Locate every blood parasite and identify its species.
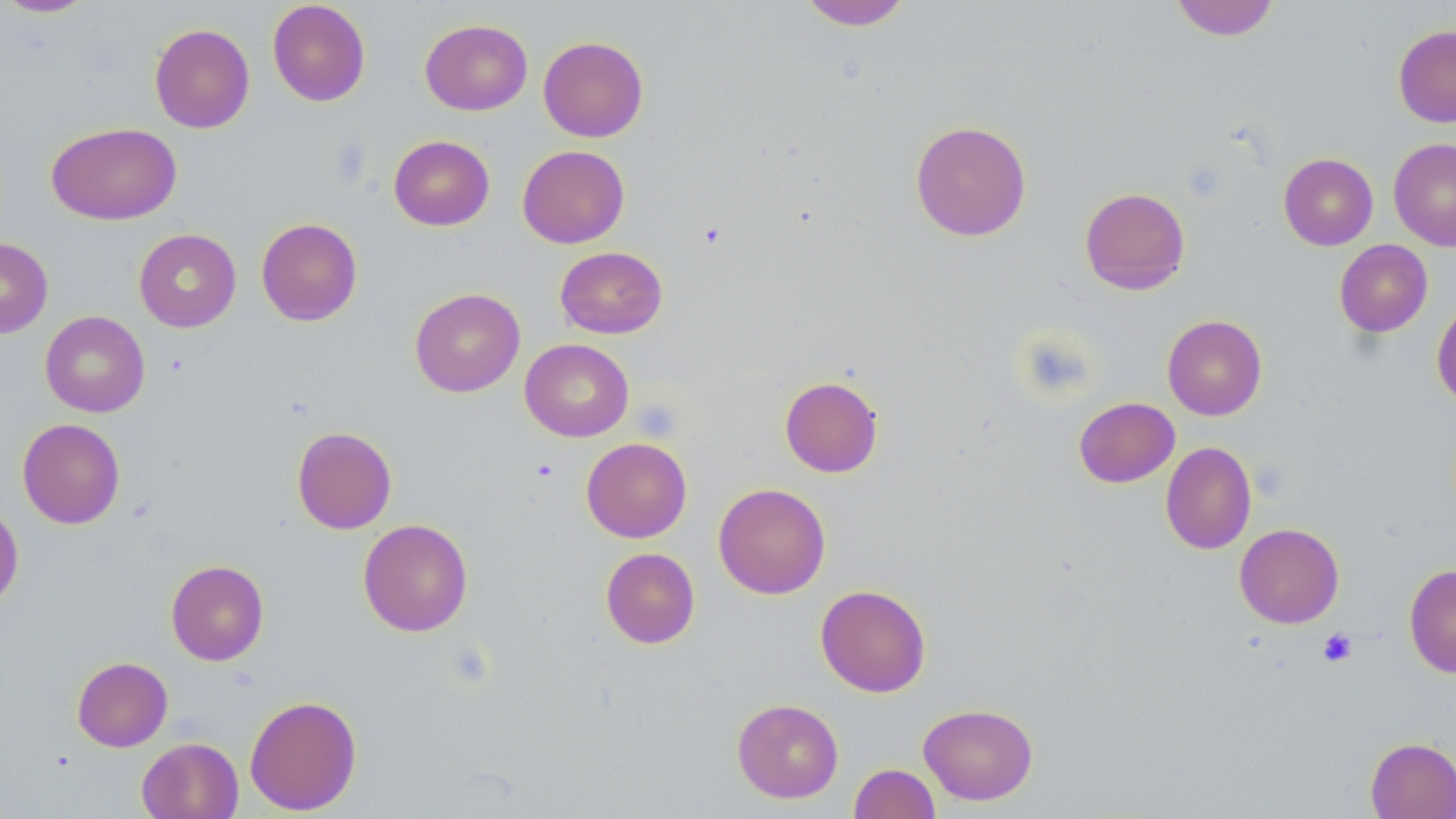
No blood parasites seen.

Summary:
  - Coordinate format: approximate bounding boxes as named x1/y1/x2/y2 corners in pixels
  - Uninfected red blood cell locations: (x1=0, y1=0, x2=97, y2=18), (x1=799, y1=0, x2=912, y2=30), (x1=1170, y1=0, x2=1279, y2=41), (x1=267, y1=1, x2=371, y2=106), (x1=420, y1=19, x2=533, y2=116), (x1=149, y1=23, x2=255, y2=133), (x1=1393, y1=25, x2=1456, y2=127), (x1=538, y1=36, x2=649, y2=142), (x1=909, y1=120, x2=1031, y2=242), (x1=46, y1=122, x2=181, y2=225), (x1=388, y1=135, x2=495, y2=231), (x1=1389, y1=138, x2=1456, y2=250), (x1=517, y1=145, x2=630, y2=248), (x1=1279, y1=153, x2=1378, y2=250), (x1=1080, y1=187, x2=1190, y2=294), (x1=256, y1=218, x2=362, y2=326), (x1=134, y1=226, x2=361, y2=327), (x1=134, y1=228, x2=241, y2=332), (x1=0, y1=237, x2=53, y2=338), (x1=1334, y1=239, x2=1433, y2=337), (x1=555, y1=246, x2=668, y2=339), (x1=410, y1=287, x2=525, y2=397), (x1=1431, y1=299, x2=1456, y2=409), (x1=40, y1=310, x2=150, y2=417), (x1=1162, y1=315, x2=1267, y2=420), (x1=520, y1=339, x2=634, y2=442), (x1=779, y1=375, x2=883, y2=478), (x1=1074, y1=397, x2=1179, y2=487), (x1=17, y1=418, x2=125, y2=529), (x1=292, y1=426, x2=397, y2=533), (x1=581, y1=437, x2=692, y2=543), (x1=1161, y1=442, x2=1256, y2=555), (x1=713, y1=483, x2=831, y2=599), (x1=0, y1=502, x2=23, y2=611), (x1=358, y1=519, x2=473, y2=636), (x1=1234, y1=523, x2=1344, y2=628), (x1=600, y1=547, x2=700, y2=649), (x1=166, y1=560, x2=269, y2=665), (x1=1404, y1=563, x2=1456, y2=678), (x1=815, y1=584, x2=931, y2=697), (x1=72, y1=656, x2=172, y2=752), (x1=244, y1=694, x2=362, y2=815), (x1=732, y1=698, x2=844, y2=803), (x1=918, y1=703, x2=1038, y2=805), (x1=136, y1=737, x2=244, y2=819), (x1=1365, y1=737, x2=1456, y2=818), (x1=849, y1=763, x2=940, y2=819)
  - Platelet locations: (x1=532, y1=458, x2=559, y2=482), (x1=1317, y1=628, x2=1357, y2=667)
  - Slide-level diagnosis: negative for blood parasites
  - Image size: 1456×819 pixels
  - Modality: optical microscopy
  - Preparation: thin blood smear
  - Magnification: 1000x
  - Field of view: single
  - Stain: May-Grünwald-Giemsa